Assess this cell for malaria.
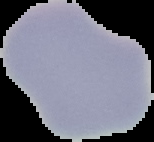

Uninfected.

preparation = thin blood smear
image size = 154×142 pixels
image type = cell region segmented out of the field of view; surrounding area masked to black